Classify this cell by malaria status.
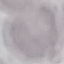

Uninfected.

{
  "image_type": "cell patch, automatically extracted from a larger field of view and resized to 64 × 64 pixels",
  "preparation": "thin smear",
  "stain": "Giemsa",
  "capture": "smartphone camera at the microscope eyepiece"
}